Locate every blood parasite and identify its species.
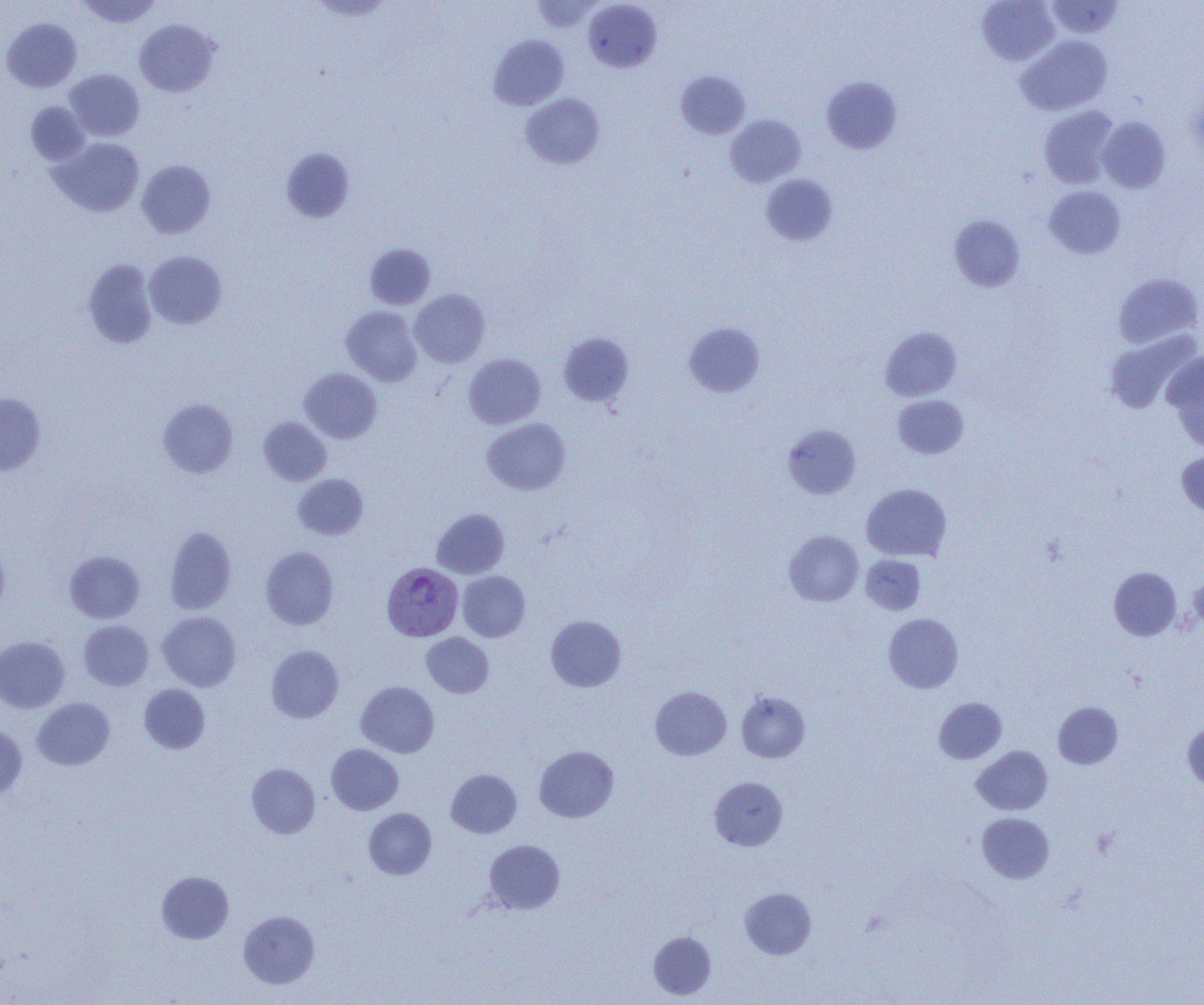
Approximate bounding boxes as (x1, y1, x2, y2) in pixels.
Plasmodium vivax-infected red blood cells: (382, 562, 462, 641).
No Plasmodium falciparum, Plasmodium ovale, Plasmodium malariae, Babesia divergens, or Trypanosoma brucei observed.

Summary:
  - Uninfected red blood cell locations: (76, 0, 162, 28), (531, 0, 603, 32), (976, 0, 1060, 65), (1045, 0, 1125, 40), (583, 1, 662, 72), (1, 18, 82, 92), (134, 19, 218, 97), (489, 34, 569, 111), (1016, 35, 1112, 115), (64, 69, 145, 141), (676, 70, 750, 139), (821, 76, 903, 153), (520, 92, 605, 169), (25, 101, 90, 165), (1039, 106, 1120, 188), (725, 114, 805, 187), (1097, 117, 1171, 193), (50, 137, 145, 217), (281, 147, 356, 223), (136, 160, 216, 238), (760, 174, 838, 245), (1044, 185, 1125, 259), (949, 214, 1026, 293), (364, 243, 436, 310), (144, 251, 227, 329), (82, 259, 158, 349), (1113, 272, 1203, 350), (410, 289, 490, 368), (340, 306, 422, 386), (683, 322, 765, 397), (880, 326, 962, 401), (1103, 330, 1200, 414), (558, 332, 634, 407), (1163, 352, 1204, 452), (463, 353, 546, 429), (299, 367, 382, 443), (0, 393, 46, 475), (893, 394, 969, 458), (158, 398, 238, 477), (258, 416, 332, 486), (482, 419, 570, 495), (782, 423, 861, 499), (1176, 451, 1204, 517), (292, 474, 368, 540), (861, 483, 952, 561), (431, 508, 509, 579), (164, 526, 237, 614), (784, 530, 864, 606), (0, 545, 10, 617), (260, 546, 338, 630), (64, 550, 145, 624), (861, 554, 925, 614), (1109, 567, 1182, 640), (458, 571, 530, 641), (1189, 575, 1204, 632), (157, 611, 241, 691), (883, 613, 963, 693), (545, 615, 626, 692), (78, 620, 153, 690), (421, 632, 494, 698), (0, 636, 69, 713), (266, 645, 344, 723), (356, 681, 439, 758), (139, 684, 211, 754), (650, 686, 731, 760), (736, 691, 810, 763), (934, 697, 1007, 764), (32, 698, 114, 770), (1053, 702, 1123, 769), (1183, 720, 1204, 790), (0, 725, 27, 800), (326, 744, 403, 815), (534, 746, 619, 822), (971, 746, 1053, 815), (246, 763, 320, 838), (446, 769, 521, 838), (709, 777, 787, 850), (364, 808, 436, 879), (977, 812, 1054, 883), (483, 839, 565, 914), (156, 871, 234, 944), (739, 888, 816, 959), (238, 910, 320, 989), (649, 931, 716, 999)
  - Slide-level diagnosis: Plasmodium vivax
  - Modality: optical microscopy
  - Magnification: 1000x
  - Image size: 1204×1005 pixels
  - Preparation: thin blood film
  - Field of view: one of a larger specimen